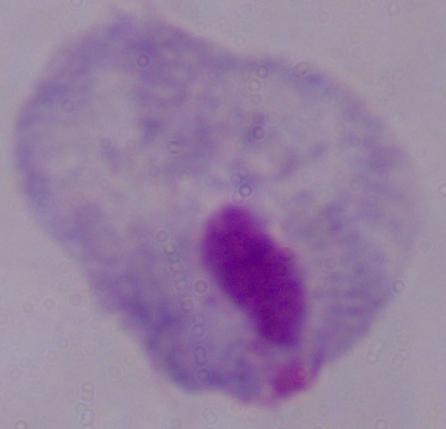 Photomicrograph. Captured at 1000x magnification. A trichomonad is shown.